Report the malaria status of this cell.
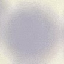
It is uninfected.

Summary:
  - Image type: automatically extracted cell patch, resized to 64 × 64 pixels
  - Preparation: thin blood smear
  - Capture: smartphone camera at the microscope eyepiece
  - Stain: Giemsa